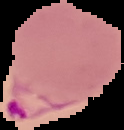
From a thin blood film. The area outside the segmented cell region is set to black. Malaria status: parasitized. Image is 124×130 pixels.